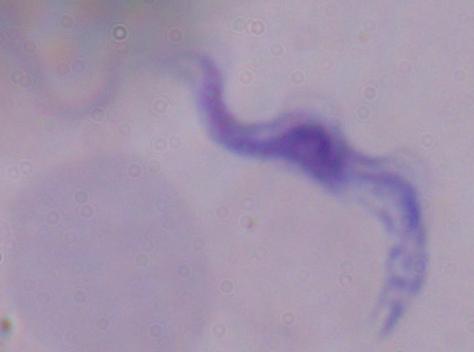

Summary:
  - Magnification: 1000x
  - Identification: trypanosome
  - Modality: micrograph